Assess this cell for malaria.
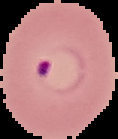
It is parasitized.

Summary:
  - Image size: 118×139 pixels
  - Preparation: thin blood smear
  - Image type: segmented cell region with the area outside set to black